Report the malaria status of this cell.
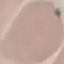

Uninfected.

Photographed with a smartphone camera at the microscope eyepiece. Giemsa-stained preparation. Thin smear of blood. Cell patch, automatically extracted from a larger field of view and resized to 64 × 64 pixels.